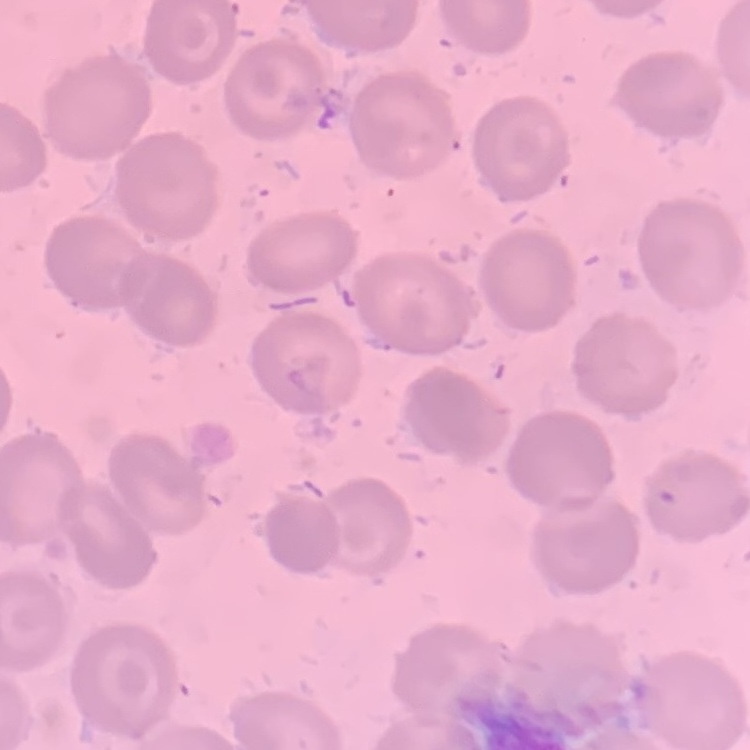 The erythrocytes show no rouleaux formation. Stained with either Field's or Giemsa. Thin peripheral smear. One tile cut from a larger photomicrograph.